Evaluate for Plasmodium parasites.
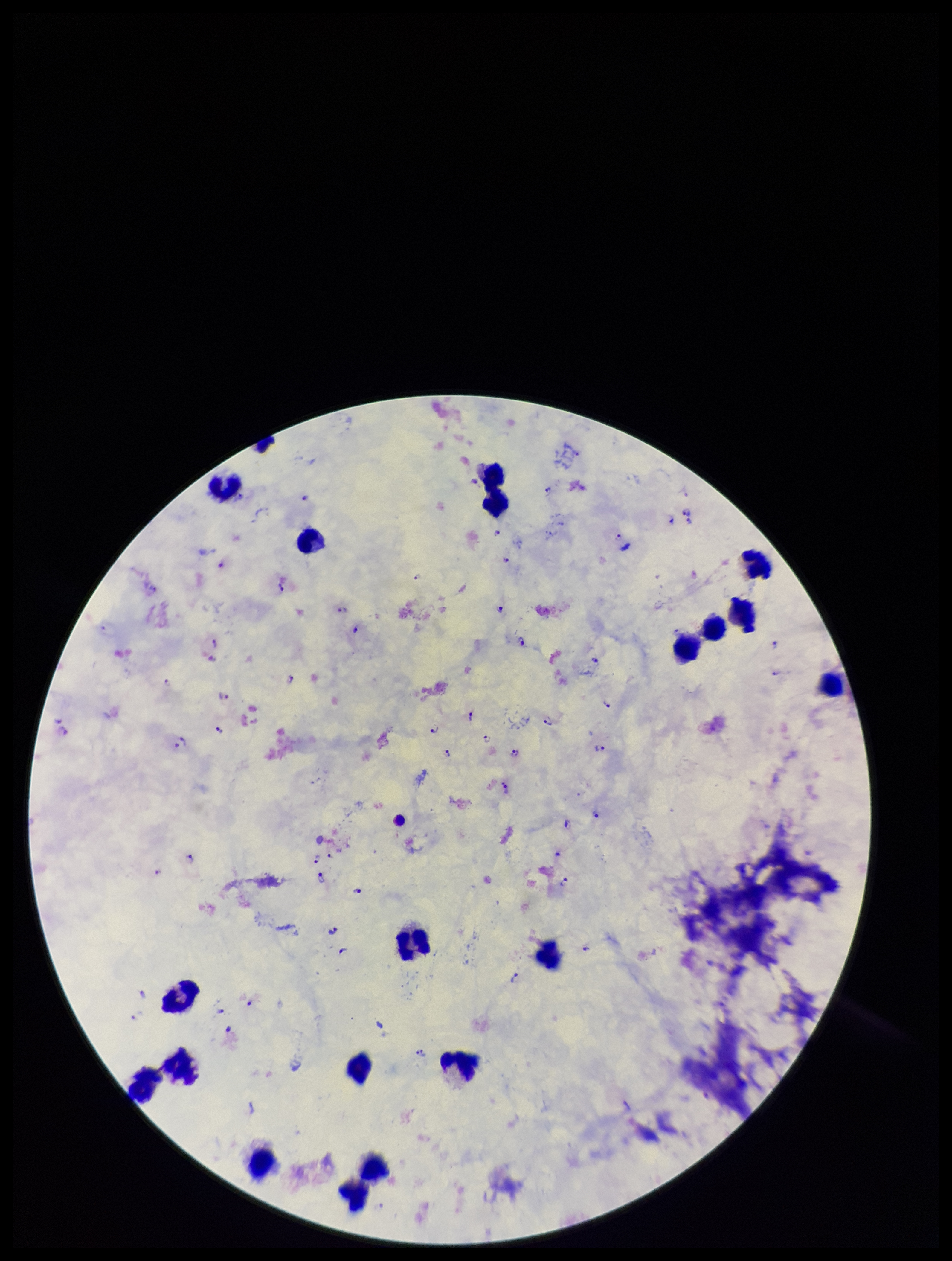
Identified.

Summary:
  - Species reported for this patient: Plasmodium falciparum
  - Preparation: thick smear
  - Parasite count: 52
  - Patient malaria status: positive
  - Capture: smartphone photograph through the microscope eyepiece
  - Stain: Giemsa
  - Leukocyte count: 19
  - Image size: 952×1261 pixels
  - Field of view: one from this slide